Comment on the morphology of the erythrocytes.
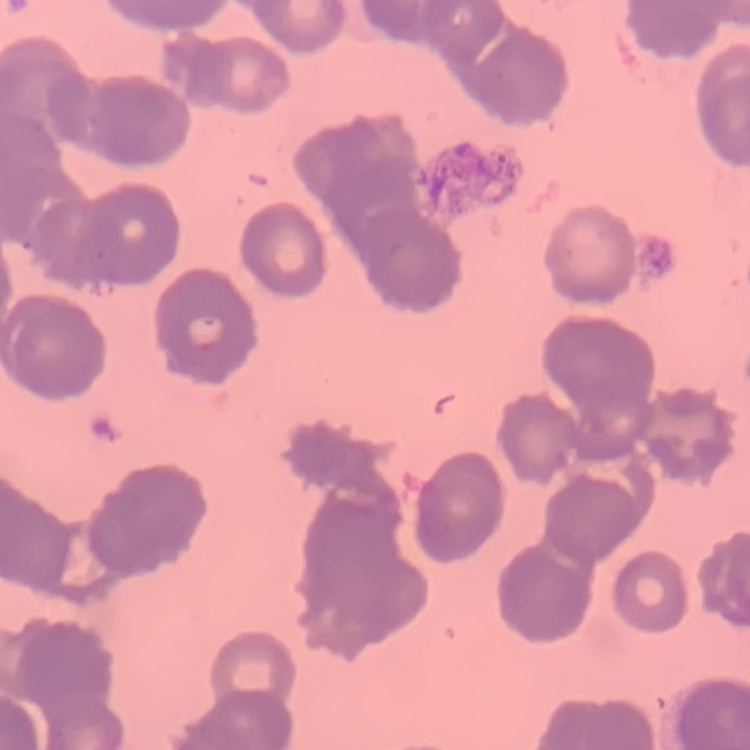

They show rouleaux formation.

Square crop of a larger photomicrograph. Stained with either Field's or Giemsa. Thin blood film.